Classify this cell by malaria status.
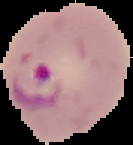
Parasitized.

image_size: 133×145 pixels
preparation: thin blood smear
image_type: segmented cell region with the area outside set to black